Comment on the morphology of the erythrocytes.
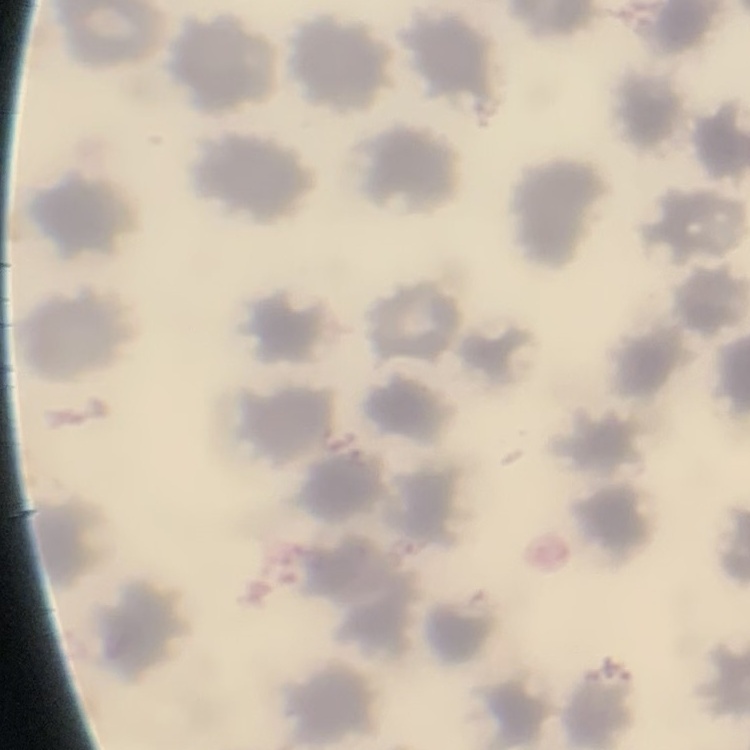
They show no rouleaux formation.

Square crop of a larger photomicrograph. Stained with either Field's or Giemsa. Thin peripheral smear.